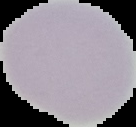 Image is 136×127 pixels. Malaria status: uninfected. From a thin blood film. The area outside the segmented cell region is set to black.